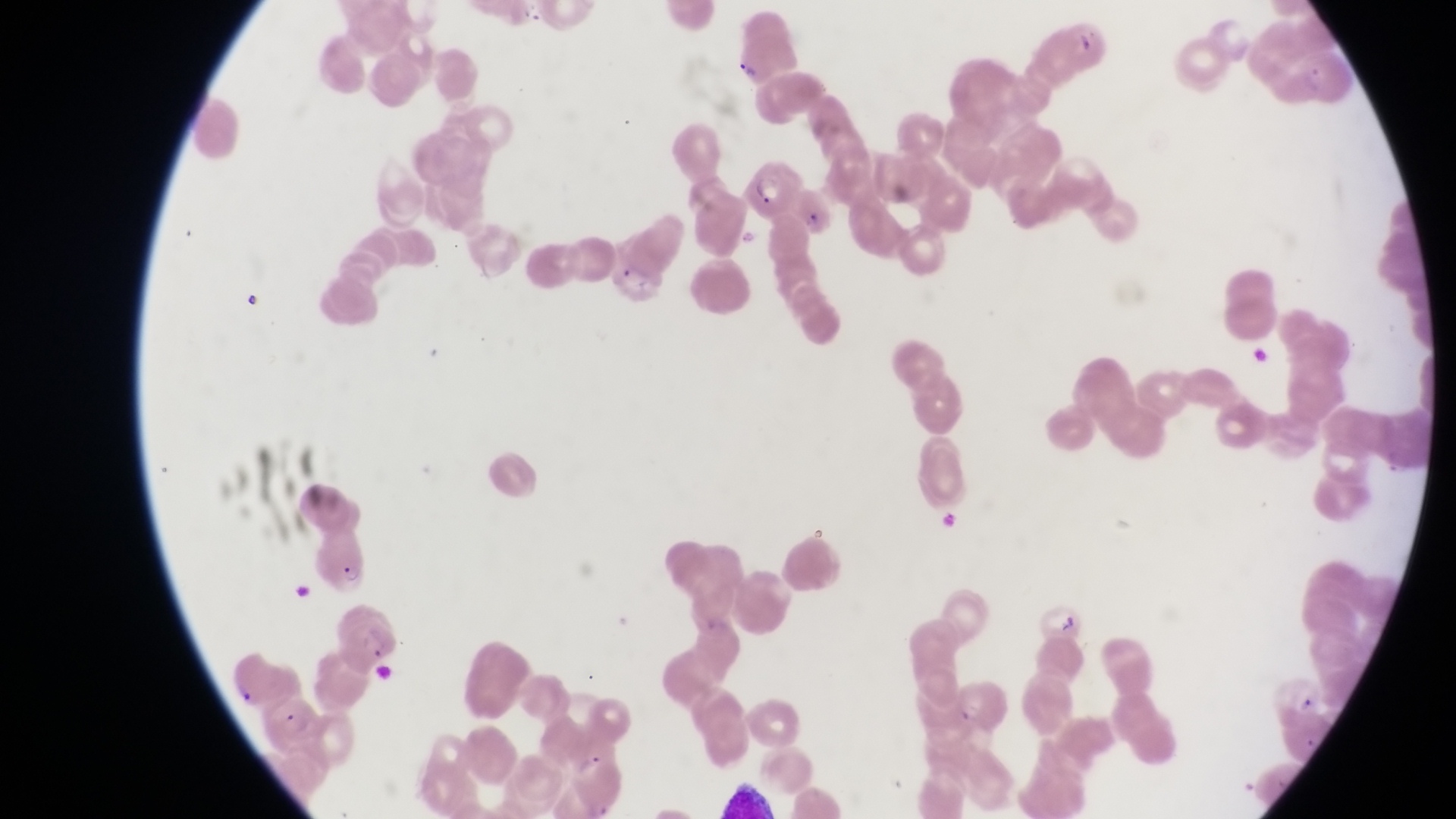
Approximate bounding boxes as [left, top, right, bottom] in pixels.
Summary:
  - Parasitised red blood cell locations: [732, 30, 796, 86], [745, 148, 800, 220], [306, 529, 367, 593], [333, 595, 399, 671], [259, 695, 325, 755]
  - Capture: smartphone photograph through the eyepiece of an Olympus CX-23 microscope
  - Preparation: thin blood smear
  - Magnification: 1000x
  - Field of view: single
  - Country: Uganda
  - Image size: 1456×819 pixels